Locate every Plasmodium parasite.
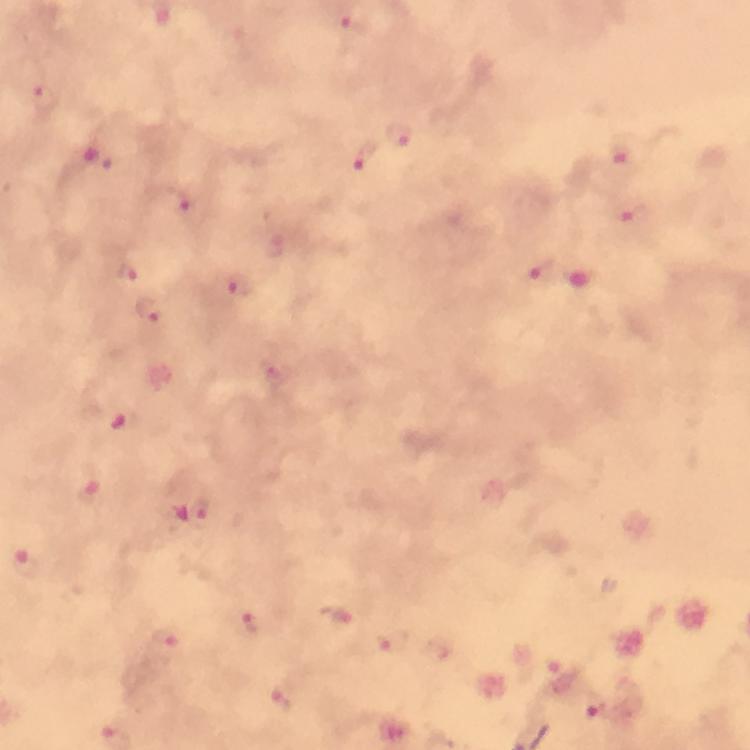
Approximate object centers, in pixels from the top-left corner.
Plasmodium parasites: (x=402, y=138), (x=629, y=154), (x=365, y=162), (x=633, y=216), (x=278, y=245), (x=538, y=272), (x=238, y=286), (x=277, y=374), (x=201, y=512), (x=25, y=556), (x=342, y=614), (x=256, y=620), (x=168, y=645), (x=286, y=700), (x=595, y=704).

capture = smartphone camera through the microscope
image size = 750×750 pixels
cropped from = a single field of view
context = from a malaria diagnostic workup
stain = Giemsa
immersion oil = used
preparation = thick blood film
magnification = 100x